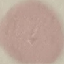

Summary:
  - Result: no malaria parasites seen
  - Stain: Giemsa
  - Preparation: thin blood film
  - Capture: smartphone through the microscope eyepiece
  - Image type: cell patch, automatically extracted from a larger field of view and resized to 64 × 64 pixels